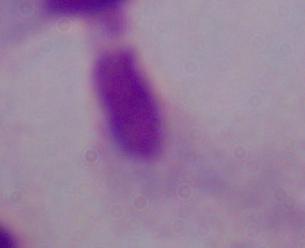
1000x magnification. Photomicrograph. A trichomonad is shown.